Report the malaria status of this cell.
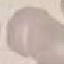
It is uninfected.

preparation = thin blood film
image type = cell patch, automatically extracted from a larger field of view and resized to 64 × 64 pixels
stain = Giemsa
capture = smartphone through the microscope eyepiece